Outline platelets.
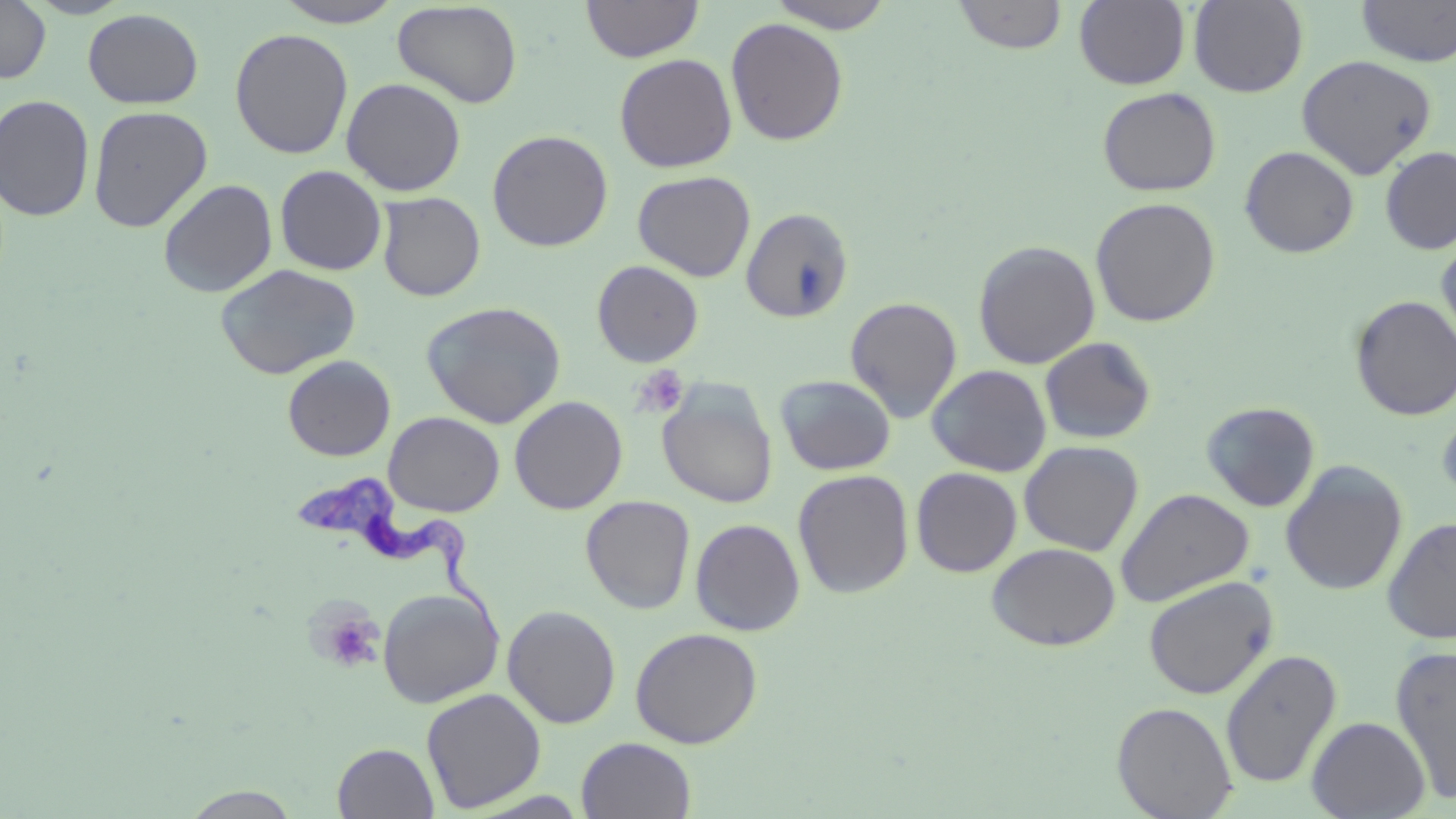

Approximate bounding boxes as named x1/y1/x2/y2 corners in pixels.
Platelets: (x1=630, y1=365, x2=690, y2=420), (x1=310, y1=601, x2=386, y2=675).

Trypanosoma brucei locations: (x1=291, y1=471, x2=502, y2=643). Uninfected red blood cell locations: (x1=581, y1=0, x2=703, y2=62), (x1=766, y1=0, x2=897, y2=33), (x1=1074, y1=0, x2=1190, y2=89), (x1=1188, y1=0, x2=1309, y2=97), (x1=1356, y1=0, x2=1456, y2=68), (x1=0, y1=1, x2=51, y2=84), (x1=272, y1=1, x2=405, y2=27), (x1=392, y1=1, x2=522, y2=109), (x1=952, y1=1, x2=1068, y2=55), (x1=83, y1=8, x2=204, y2=109), (x1=726, y1=17, x2=849, y2=146), (x1=229, y1=28, x2=354, y2=159), (x1=614, y1=53, x2=737, y2=172), (x1=1295, y1=54, x2=1437, y2=179), (x1=341, y1=77, x2=466, y2=196), (x1=1098, y1=87, x2=1221, y2=197), (x1=0, y1=94, x2=95, y2=221), (x1=88, y1=105, x2=212, y2=232), (x1=487, y1=129, x2=613, y2=251), (x1=1239, y1=145, x2=1360, y2=258), (x1=1380, y1=145, x2=1456, y2=255), (x1=275, y1=165, x2=387, y2=276), (x1=633, y1=170, x2=755, y2=281), (x1=157, y1=178, x2=278, y2=298), (x1=376, y1=192, x2=486, y2=302), (x1=1090, y1=197, x2=1221, y2=328), (x1=741, y1=207, x2=854, y2=323), (x1=1436, y1=231, x2=1456, y2=353), (x1=973, y1=240, x2=1100, y2=369), (x1=592, y1=260, x2=705, y2=367), (x1=215, y1=264, x2=361, y2=379), (x1=1349, y1=295, x2=1456, y2=421), (x1=845, y1=296, x2=962, y2=423), (x1=421, y1=300, x2=567, y2=428), (x1=1038, y1=336, x2=1157, y2=445), (x1=282, y1=355, x2=396, y2=461), (x1=927, y1=364, x2=1052, y2=477), (x1=775, y1=374, x2=896, y2=475), (x1=658, y1=386, x2=777, y2=508), (x1=509, y1=396, x2=628, y2=514), (x1=1435, y1=397, x2=1456, y2=509), (x1=1201, y1=401, x2=1321, y2=513), (x1=384, y1=411, x2=505, y2=517), (x1=1019, y1=440, x2=1143, y2=556), (x1=1280, y1=461, x2=1408, y2=596), (x1=911, y1=467, x2=1023, y2=577), (x1=793, y1=469, x2=914, y2=598), (x1=1115, y1=488, x2=1254, y2=608), (x1=580, y1=495, x2=696, y2=614), (x1=1382, y1=516, x2=1456, y2=645), (x1=690, y1=518, x2=806, y2=636), (x1=986, y1=542, x2=1121, y2=651), (x1=1143, y1=576, x2=1278, y2=700), (x1=377, y1=587, x2=503, y2=708), (x1=502, y1=604, x2=621, y2=729), (x1=630, y1=627, x2=763, y2=748), (x1=1390, y1=644, x2=1456, y2=805), (x1=1220, y1=649, x2=1342, y2=789), (x1=421, y1=687, x2=546, y2=812), (x1=1112, y1=701, x2=1238, y2=818), (x1=1306, y1=716, x2=1430, y2=818), (x1=577, y1=737, x2=696, y2=819), (x1=332, y1=742, x2=439, y2=818), (x1=177, y1=786, x2=305, y2=818). Slide-level diagnosis: Trypanosoma brucei. May-Grünwald-Giemsa-stained preparation. Thin blood film. Light microscopy. One field of a larger specimen. Captured at 1000x magnification. Image is 1456×819 pixels.